Assess this cell for malaria.
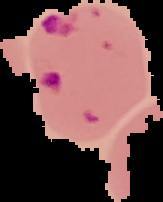

It is parasitized.

Summary:
  - Preparation: thin blood smear
  - Image type: segmented cell region with the area outside set to black
  - Image size: 163×202 pixels